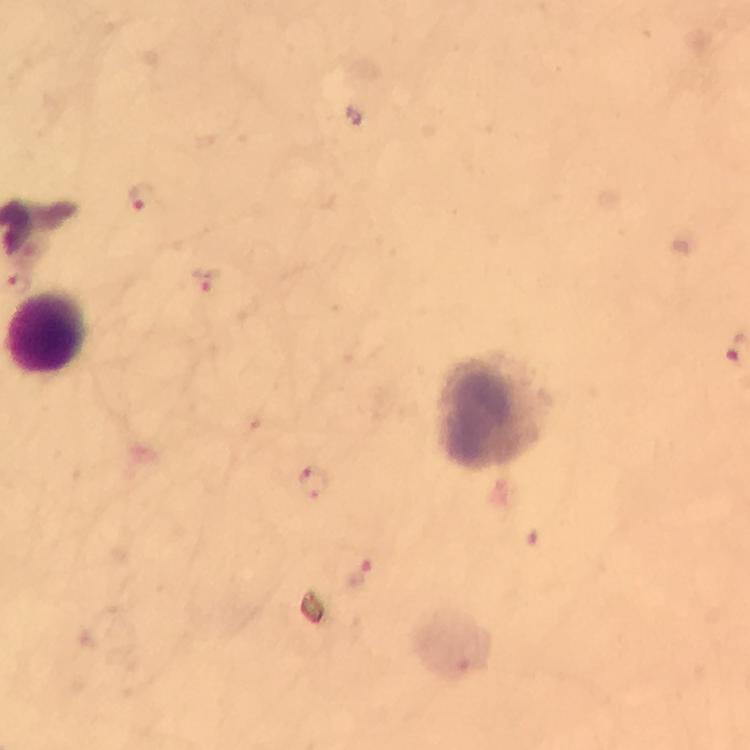
Approximate centers as [x, y] in pixels. Plasmodium parasite locations: [142, 199], [208, 279], [310, 486], [359, 574]. Leukocyte locations: [45, 336], [491, 411]. At 100x magnification. Immersion oil was used. Thick blood film. Giemsa-stained preparation. Smartphone photograph taken through a microscope. A crop from one field of view. Image is 750×750 pixels. From a malaria diagnostic workup.